Give the position of each Plasmodium falciparum parasite with its life-cycle stage, each leukocyte, and any debris.
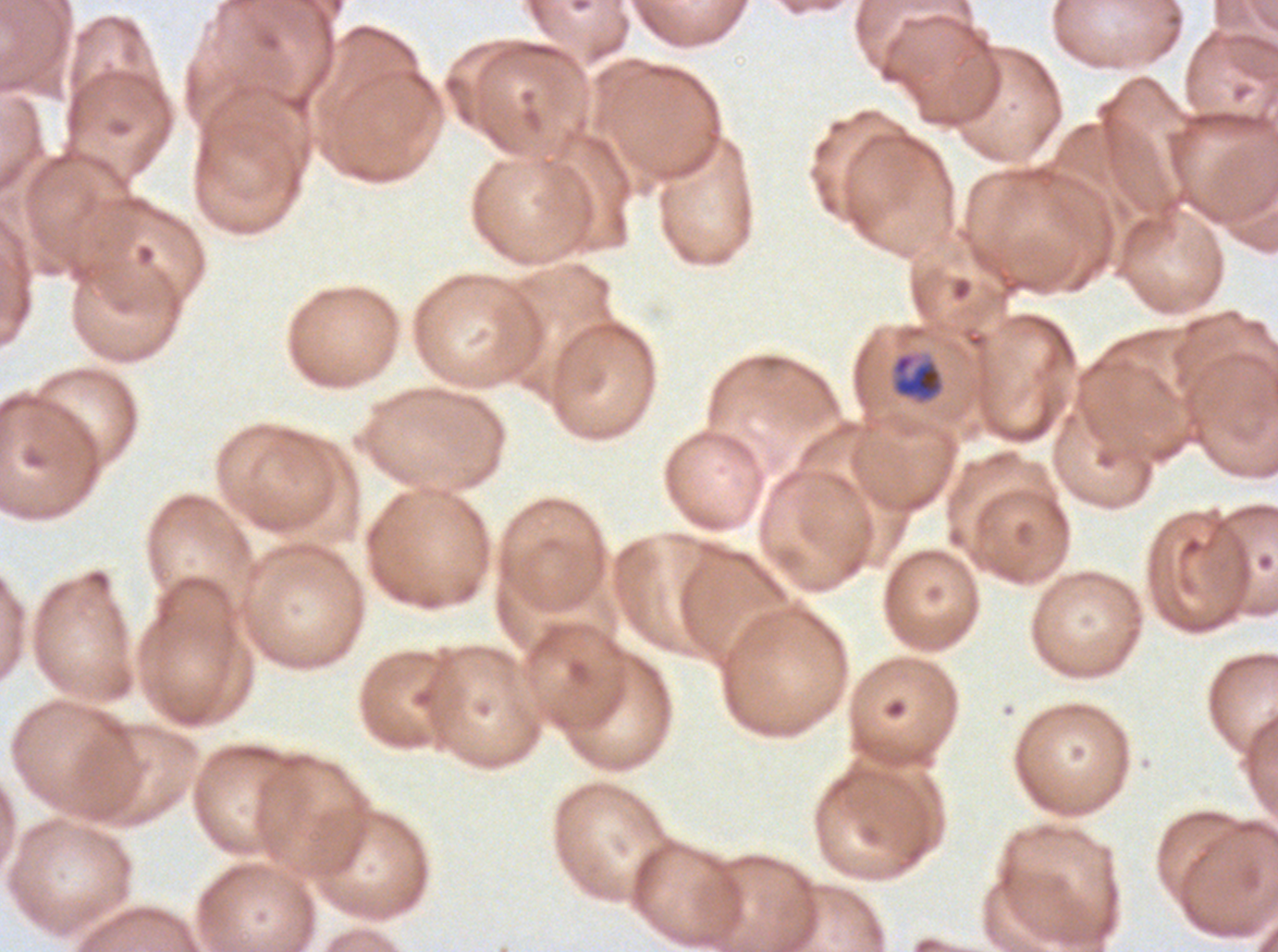
Approximate bounding boxes as (x1, y1, x2, y2) in pixels.
Late-ring/early-trophozoite forms: (891, 352, 944, 403).
No rings, mid trophozoites, late trophozoites, early schizonts, late schizonts, segmenters, gametocytes, leukocytes, or debris observed.

Summary:
  - Stain: Giemsa
  - Preparation: thin blood film
  - Specimen: ex-vivo Plasmodium falciparum culture from a patient in The Gambia, grown for 24 to 48 hours
  - Field of view: one sub-image of a larger composite
  - Image size: 1278×952 pixels